Assess this cell for malaria.
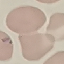

Uninfected.

Summary:
  - Image type: cell patch, automatically extracted from a larger field of view and resized to 64 × 64 pixels
  - Stain: Giemsa
  - Preparation: thin blood film
  - Capture: smartphone camera at the microscope eyepiece